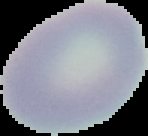

Summary:
  - Image size: 148×136 pixels
  - Image type: segmented cell region on a black background
  - Preparation: thin blood film
  - Result: no Plasmodium parasites detected